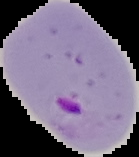

preparation = thin blood film
result = Plasmodium parasites identified
image size = 139×157 pixels
image type = cell region segmented out of the field of view; surrounding area masked to black